Outline each blood parasite and name the species.
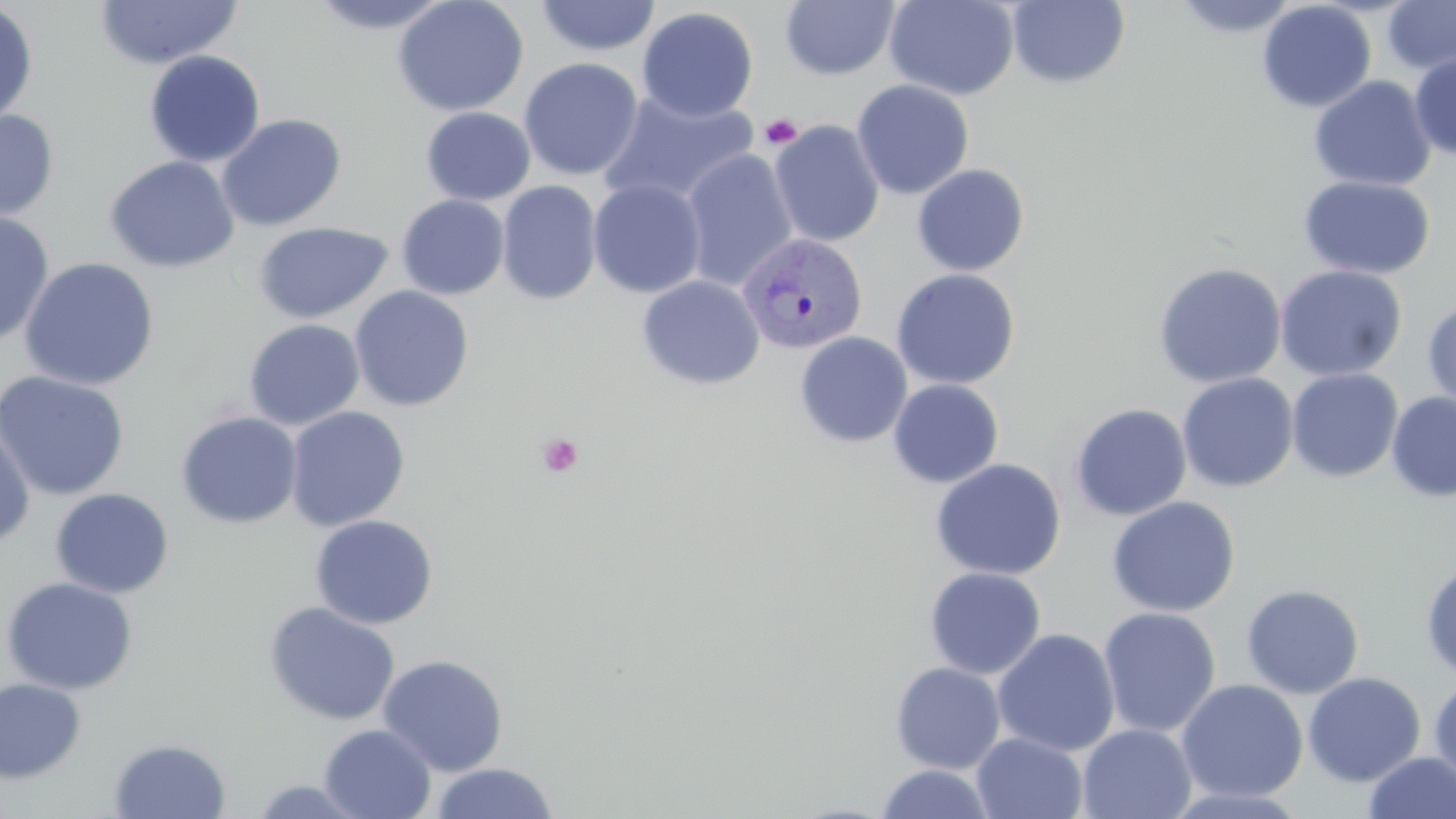

Approximate bounding boxes as (x1, y1, x2, y2) in pixels.
Plasmodium vivax-infected red blood cells: (738, 233, 868, 355).
No Plasmodium falciparum, Plasmodium ovale, Plasmodium malariae, Babesia divergens, or Trypanosoma brucei observed.

slide-level diagnosis = Plasmodium vivax
field of view = one of a larger specimen
platelet locations = approximate bounding boxes as (x1, y1, x2, y2) in pixels: (759, 114, 803, 149), (538, 433, 584, 478)
image size = 1456×819 pixels
preparation = thin blood film
magnification = 1000x
uninfected red blood cell locations = approximate bounding boxes as (x1, y1, x2, y2) in pixels: (306, 0, 456, 35), (392, 0, 529, 117), (534, 0, 661, 58), (884, 0, 1020, 100), (1170, 0, 1301, 39), (93, 1, 243, 69), (780, 1, 900, 80), (1007, 1, 1131, 89), (1256, 1, 1377, 113), (1381, 1, 1456, 76), (0, 2, 39, 127), (636, 7, 759, 122), (143, 49, 266, 168), (1409, 50, 1456, 160), (519, 57, 644, 181), (1308, 75, 1436, 192), (851, 80, 974, 199), (596, 90, 760, 209), (420, 106, 536, 206), (0, 108, 59, 222), (216, 113, 347, 232), (768, 120, 885, 248), (680, 148, 798, 290), (104, 155, 239, 273), (911, 163, 1029, 276), (1298, 175, 1435, 280), (588, 178, 707, 298), (496, 180, 602, 305), (397, 194, 510, 299), (0, 211, 55, 347), (252, 221, 394, 324), (19, 257, 160, 391), (1152, 261, 1287, 389), (1274, 264, 1408, 381), (891, 268, 1020, 390), (637, 275, 765, 390), (349, 286, 474, 412), (1422, 299, 1456, 413), (243, 318, 365, 430), (794, 331, 912, 448), (1286, 368, 1403, 483), (0, 371, 130, 501), (1176, 372, 1298, 492), (887, 379, 1004, 488), (1386, 391, 1456, 502), (1069, 403, 1192, 521), (284, 406, 410, 532), (175, 411, 303, 529), (0, 418, 35, 550), (930, 458, 1066, 580), (50, 488, 174, 599), (1106, 496, 1240, 617), (309, 514, 438, 630), (1420, 559, 1456, 681), (924, 567, 1046, 680), (1, 577, 138, 695), (1241, 584, 1365, 699), (263, 601, 400, 726), (1098, 606, 1221, 738), (992, 628, 1120, 757), (377, 653, 509, 776), (889, 661, 1006, 774), (1303, 672, 1426, 787), (0, 677, 86, 783), (1428, 677, 1456, 790), (1176, 679, 1308, 802), (318, 723, 436, 819), (1077, 723, 1197, 819), (971, 732, 1088, 818), (108, 737, 231, 818), (1361, 751, 1456, 819), (429, 762, 560, 819), (873, 764, 997, 819), (245, 777, 375, 818)
stain = May-Grünwald-Giemsa
modality = optical microscopy